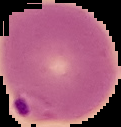
Summary:
  - Malaria status: parasitized
  - Image size: 121×127 pixels
  - Preparation: thin blood film
  - Image type: segmented cell region with the area outside set to black